Report the malaria status of this cell.
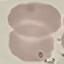

It is uninfected.

Summary:
  - Image type: cell patch, automatically extracted from a larger field of view and resized to 64 × 64 pixels
  - Stain: Giemsa
  - Preparation: thin blood smear
  - Capture: smartphone camera at the microscope eyepiece